Report the malaria status of this cell.
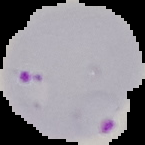
It is parasitized.

Summary:
  - Preparation: thin blood film
  - Image type: cell region segmented out of the field of view; surrounding area masked to black
  - Image size: 145×145 pixels